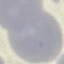

{
  "result": "negative for malaria parasites",
  "image_type": "automatically extracted cell patch, resized to 64 × 64 pixels",
  "capture": "smartphone through the microscope eyepiece",
  "preparation": "thin blood film",
  "stain": "Giemsa"
}